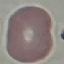 Malaria status: uninfected. Photographed with a smartphone camera at the microscope eyepiece. Giemsa-stained preparation. Thin blood film. Automatically extracted cell patch, resized to 64 × 64 pixels.